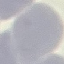
Result: negative for malaria parasites. Thin blood smear. Giemsa stain. Automatically extracted cell patch, resized to 64 × 64 pixels. Photographed with a smartphone camera at the microscope eyepiece.